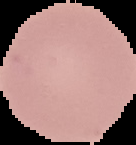

{
  "image_type": "cell region segmented out of the field of view; surrounding area masked to black",
  "preparation": "thin blood film",
  "malaria_status": "uninfected",
  "image_size": "136×145 pixels"
}